Comment on the morphology of the red blood cells.
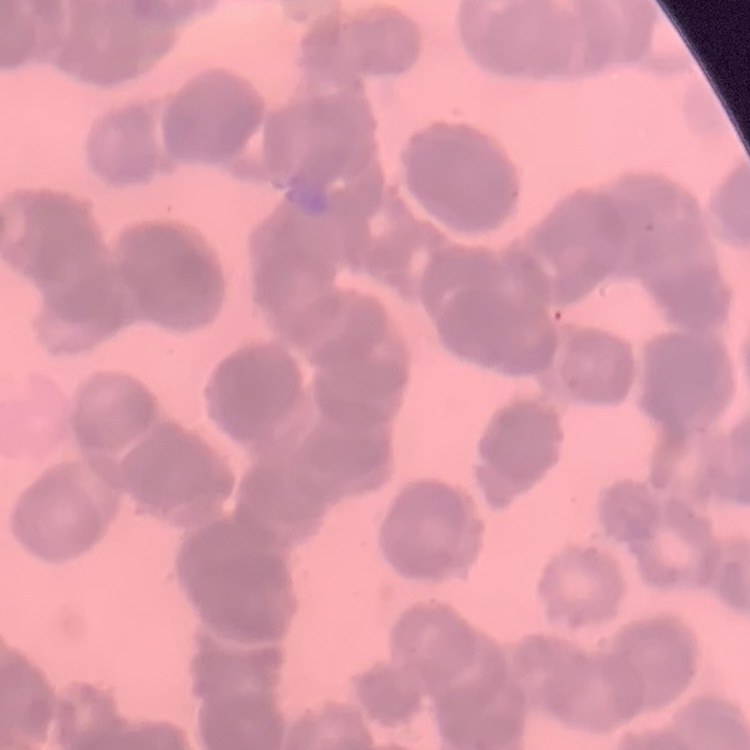

Rouleaux formation.

preparation = thin blood film
stain = Field's or Giemsa
image type = one tile cut from a larger photomicrograph